Classify this cell by malaria status.
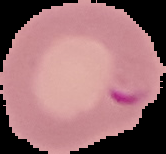
It is parasitized.

Cell region segmented out of the field of view; the surrounding area is masked to black. Image is 166×154 pixels. From a thin blood film.